Assess the morphology of the erythrocytes.
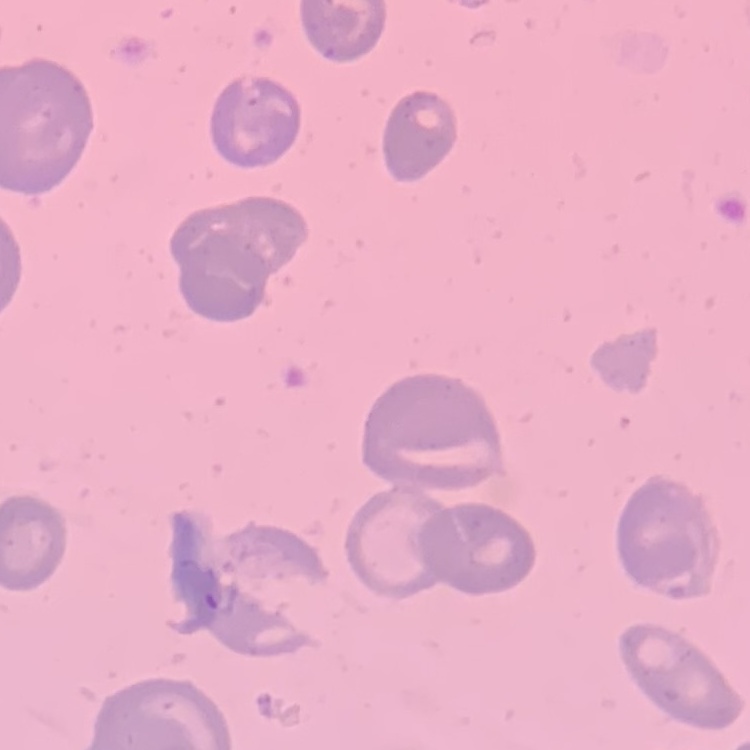

No rouleaux formation.

Summary:
  - Stain: Field's or Giemsa
  - Image type: one tile cut from a larger photomicrograph
  - Preparation: thin peripheral smear